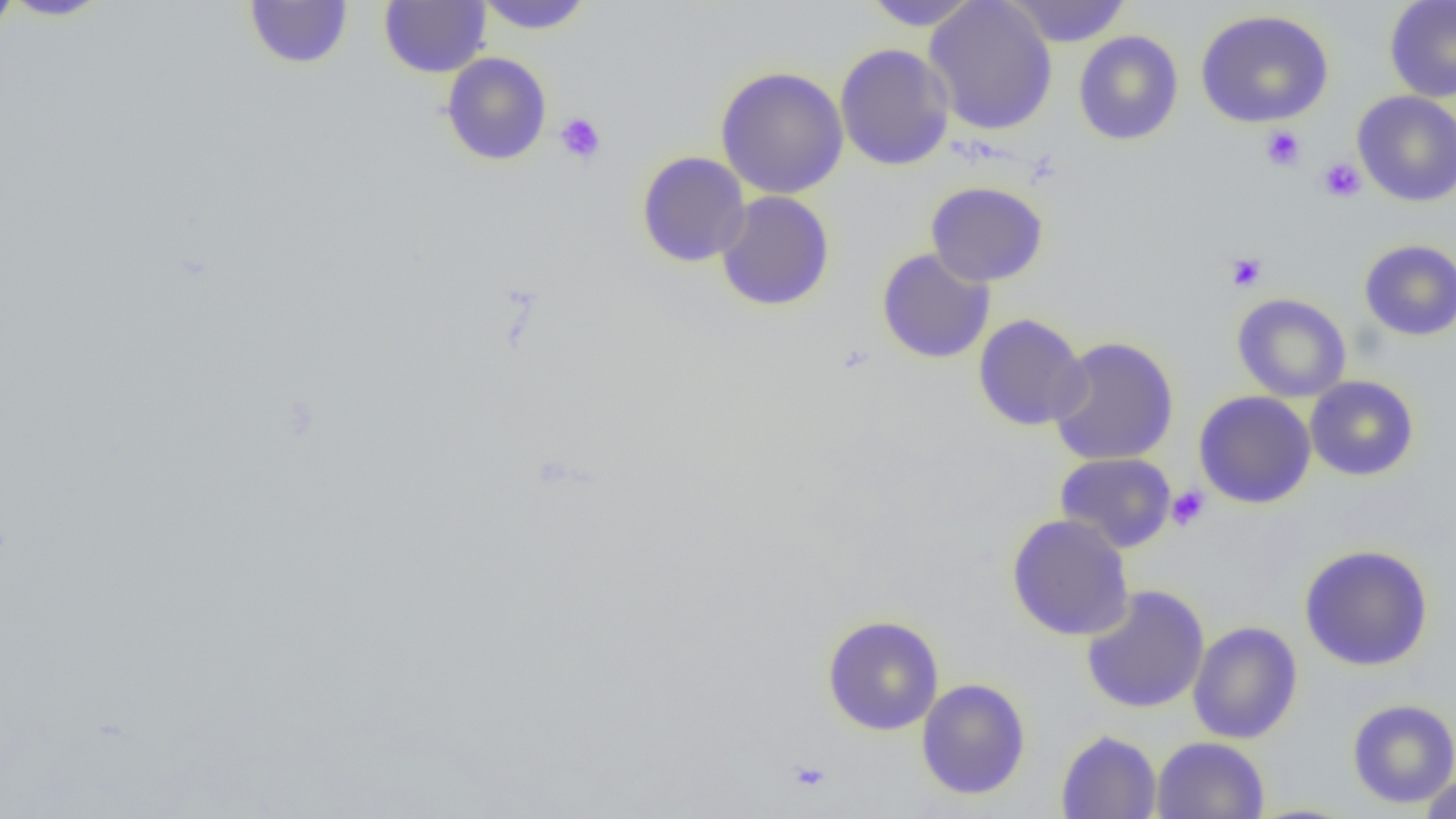

Approximate bounding boxes as (x1,y1)-(x2,y2) corner pairs in pixels. Uninfected red blood cell locations: (0,0)-(21,42), (1,0)-(115,21), (244,0)-(354,70), (379,0)-(490,78), (474,0)-(595,34), (860,0)-(982,30), (923,0)-(1058,136), (1003,0)-(1132,47), (1384,0)-(1456,103), (1195,9)-(1334,128), (1073,30)-(1184,146), (834,43)-(955,171), (441,52)-(552,166), (714,66)-(849,199), (1353,91)-(1456,207), (636,151)-(750,267), (925,181)-(1049,287), (715,191)-(835,312), (1359,239)-(1456,341), (876,248)-(995,364), (1232,293)-(1352,402), (973,313)-(1090,431), (1047,336)-(1179,467), (1305,375)-(1419,481), (1193,391)-(1316,509), (1054,453)-(1177,554), (1006,514)-(1135,641), (1299,544)-(1434,671), (1081,584)-(1210,715), (822,615)-(944,735), (1187,621)-(1303,744), (916,678)-(1031,799), (1347,698)-(1456,809), (1056,729)-(1162,819), (1152,736)-(1269,819), (1418,774)-(1456,818). Platelet locations: (554,112)-(607,165), (1260,125)-(1306,171), (1317,157)-(1366,203), (1226,252)-(1267,292), (1166,486)-(1210,531), (788,760)-(832,796). Slide-level diagnosis: negative for blood parasites. Captured at 1000x magnification. Light microscopy. Thin blood film. One field of a larger specimen. Image is 1456×819 pixels.